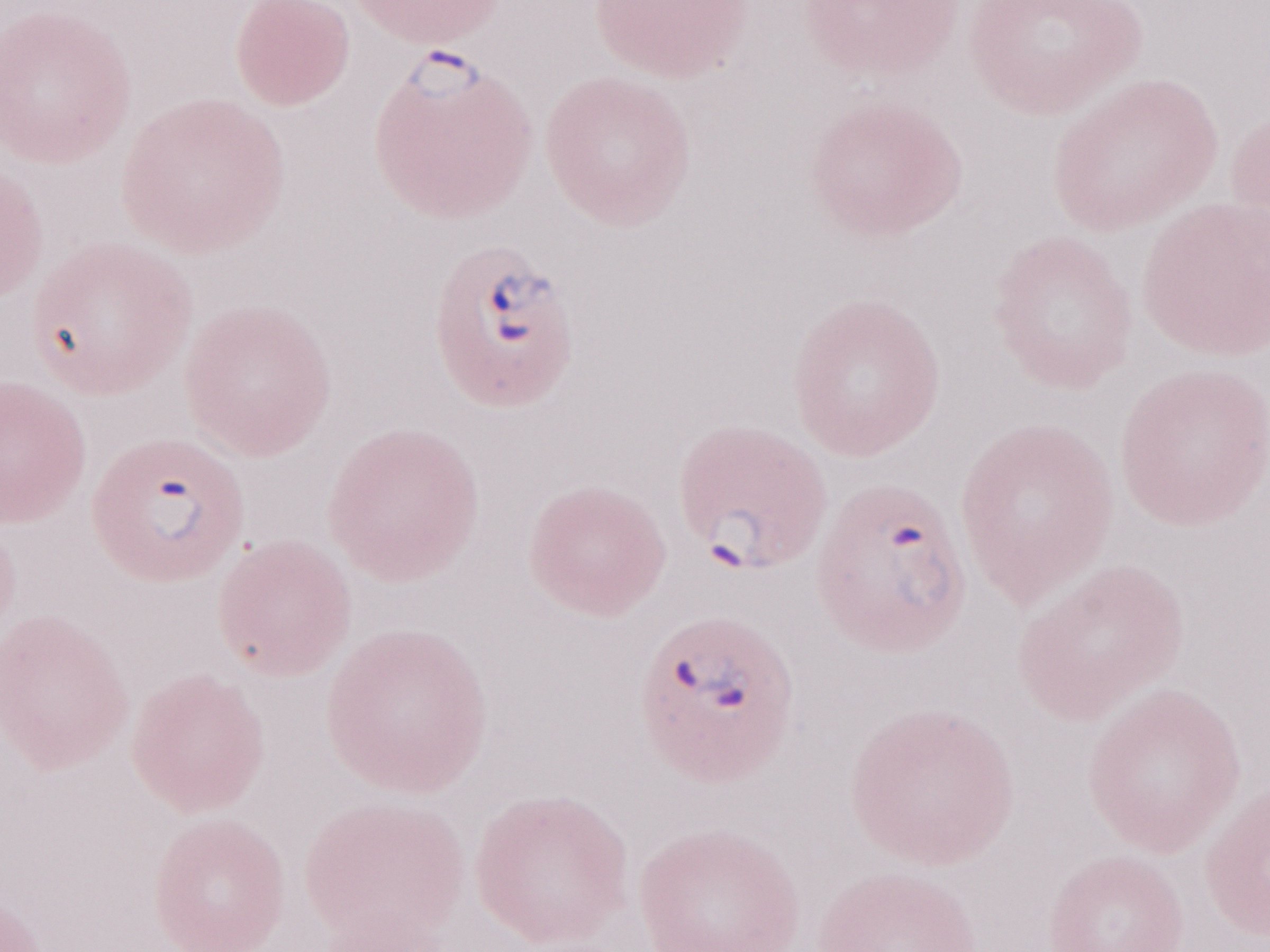
Olympus BX43 microscope and DP73 digital camera. Patient-level malaria diagnosis: positive. May-Grünwald-Giemsa-stained preparation. One field of this slide. Magnification: 1,000x. Image is 1270×952 pixels. Thin peripheral-blood smear.